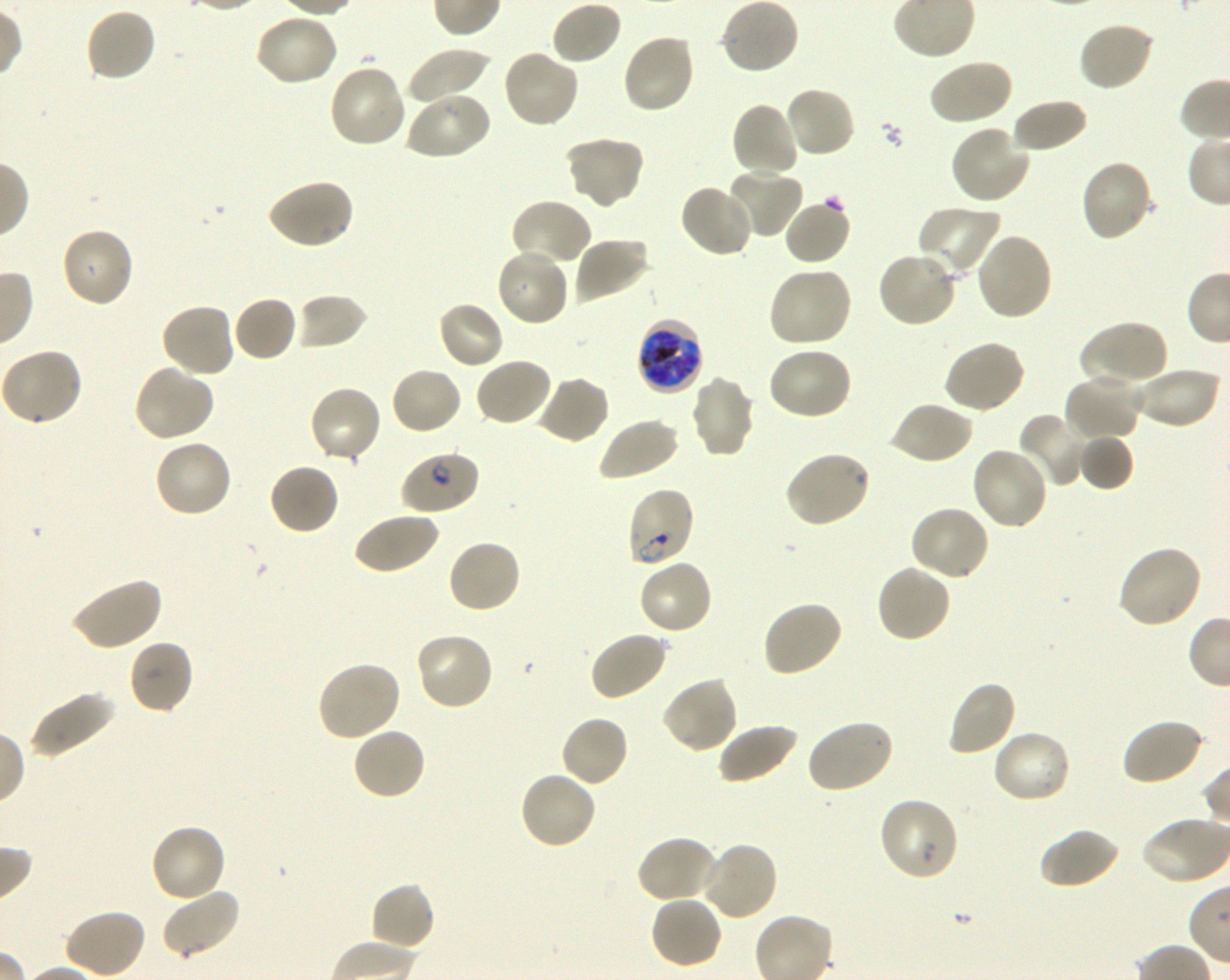
Approximate bounding rectangles given as corner coordinates in pixels from the top-left. Not every red blood cell is marked. A life-cycle stage — or a range of stages, where the recorded stages span more than one — follows each staged infected red blood cell. Locations of uninfected red blood cells: (x1=550, y1=0, x2=623, y2=66), (x1=720, y1=0, x2=800, y2=76), (x1=84, y1=7, x2=158, y2=82), (x1=254, y1=13, x2=339, y2=88), (x1=1077, y1=21, x2=1155, y2=92), (x1=621, y1=32, x2=696, y2=115), (x1=406, y1=46, x2=492, y2=105), (x1=501, y1=48, x2=580, y2=129), (x1=927, y1=58, x2=1013, y2=127), (x1=327, y1=63, x2=407, y2=150), (x1=783, y1=86, x2=856, y2=159), (x1=404, y1=90, x2=491, y2=161), (x1=1011, y1=97, x2=1088, y2=153), (x1=730, y1=101, x2=801, y2=180), (x1=950, y1=124, x2=1031, y2=205), (x1=563, y1=134, x2=645, y2=210), (x1=1078, y1=158, x2=1155, y2=242), (x1=725, y1=167, x2=804, y2=239), (x1=265, y1=177, x2=355, y2=251), (x1=678, y1=183, x2=754, y2=258), (x1=783, y1=197, x2=852, y2=266), (x1=509, y1=199, x2=592, y2=269), (x1=916, y1=204, x2=1001, y2=278), (x1=59, y1=227, x2=135, y2=309), (x1=975, y1=233, x2=1053, y2=321), (x1=573, y1=237, x2=650, y2=304), (x1=495, y1=247, x2=570, y2=328), (x1=876, y1=249, x2=958, y2=329), (x1=766, y1=267, x2=853, y2=349), (x1=294, y1=293, x2=368, y2=351), (x1=232, y1=295, x2=299, y2=363), (x1=436, y1=300, x2=505, y2=371), (x1=160, y1=302, x2=236, y2=378), (x1=1078, y1=319, x2=1168, y2=389), (x1=942, y1=339, x2=1026, y2=415), (x1=765, y1=347, x2=853, y2=422), (x1=1, y1=348, x2=82, y2=430), (x1=474, y1=357, x2=553, y2=428), (x1=131, y1=364, x2=216, y2=443), (x1=390, y1=366, x2=463, y2=435), (x1=1134, y1=367, x2=1222, y2=430), (x1=1064, y1=372, x2=1144, y2=442), (x1=534, y1=374, x2=611, y2=445), (x1=689, y1=376, x2=756, y2=458), (x1=308, y1=385, x2=383, y2=465), (x1=889, y1=400, x2=974, y2=465), (x1=1017, y1=412, x2=1091, y2=487), (x1=598, y1=417, x2=680, y2=482), (x1=1078, y1=433, x2=1133, y2=491), (x1=152, y1=438, x2=233, y2=518), (x1=970, y1=446, x2=1050, y2=532), (x1=268, y1=462, x2=340, y2=536), (x1=909, y1=505, x2=990, y2=583), (x1=352, y1=510, x2=439, y2=575), (x1=446, y1=538, x2=522, y2=614), (x1=1116, y1=544, x2=1204, y2=630), (x1=637, y1=558, x2=714, y2=636), (x1=875, y1=564, x2=952, y2=644), (x1=69, y1=576, x2=163, y2=651), (x1=760, y1=600, x2=844, y2=678), (x1=589, y1=631, x2=669, y2=702), (x1=413, y1=632, x2=495, y2=711), (x1=127, y1=638, x2=195, y2=714), (x1=316, y1=660, x2=401, y2=742), (x1=661, y1=676, x2=739, y2=754), (x1=945, y1=679, x2=1017, y2=757), (x1=28, y1=689, x2=115, y2=759), (x1=560, y1=714, x2=629, y2=787), (x1=805, y1=718, x2=894, y2=794), (x1=1121, y1=718, x2=1205, y2=786), (x1=717, y1=722, x2=799, y2=786), (x1=351, y1=726, x2=427, y2=803), (x1=991, y1=729, x2=1073, y2=805), (x1=518, y1=769, x2=598, y2=850), (x1=877, y1=796, x2=960, y2=882), (x1=150, y1=824, x2=228, y2=904), (x1=1040, y1=827, x2=1121, y2=890), (x1=636, y1=835, x2=719, y2=904), (x1=699, y1=841, x2=779, y2=922), (x1=368, y1=882, x2=436, y2=952), (x1=160, y1=887, x2=241, y2=959), (x1=649, y1=895, x2=723, y2=970), (x1=64, y1=908, x2=147, y2=978). Locations of infected red blood cells: (x1=636, y1=318, x2=705, y2=394) late trophozoite to late schizont; (x1=625, y1=486, x2=696, y2=568) ring. Locations of red blood cells of indeterminate infection status: (x1=399, y1=451, x2=480, y2=516), (x1=783, y1=451, x2=871, y2=529). 100x objective under oil immersion, numerical aperture 1.30. One field from this slide. Thin blood smear. P. falciparum strain 3D7 in shaking in-vitro culture. Donor blood group O+. Giemsa-stained preparation. Image is 1230×980 pixels.